Comment on the morphology of the red blood cells.
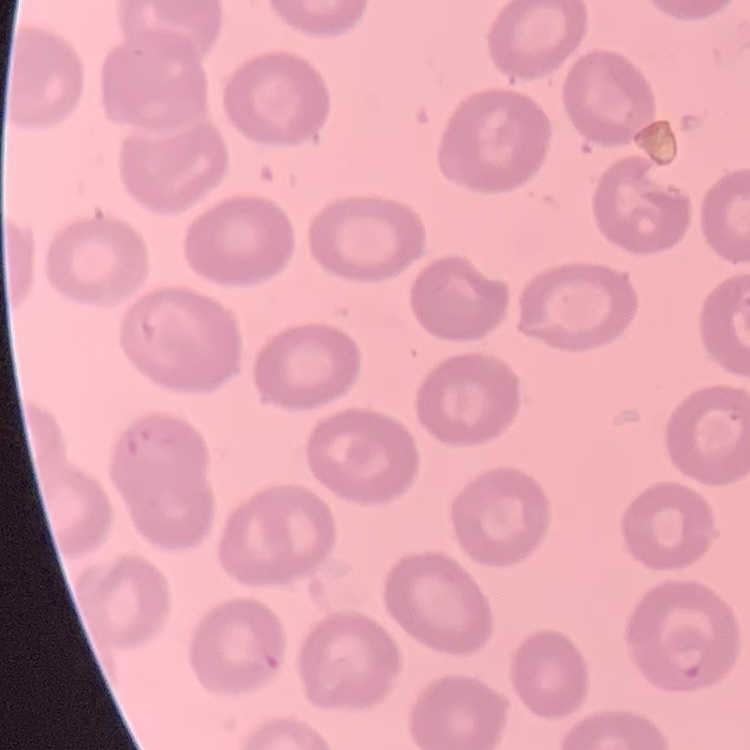
No rouleaux formation.

Thin blood film. One tile cut from a larger photomicrograph. Field's or Giemsa stain.